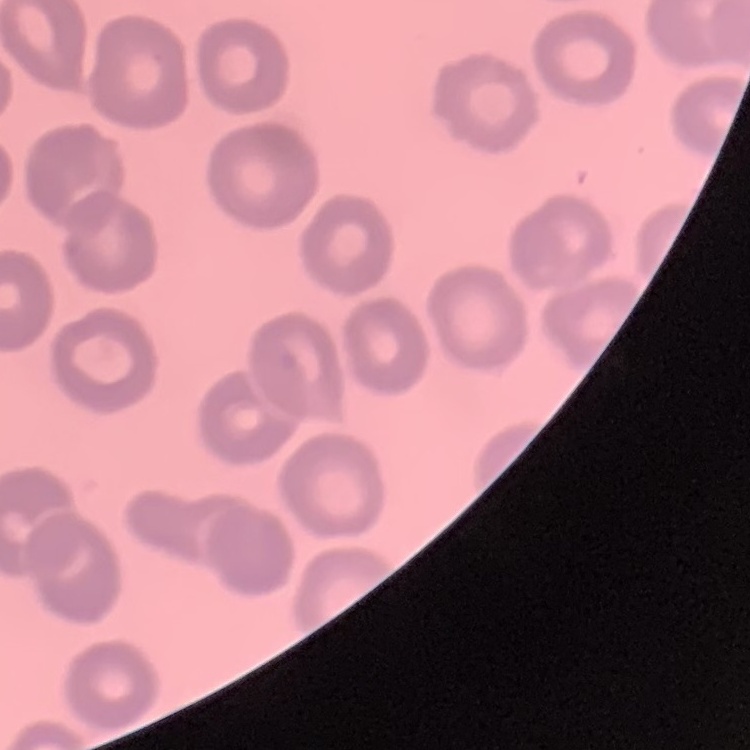
{
  "red_blood_cell_morphology": "no rouleaux formation",
  "image_type": "square crop of a larger photomicrograph",
  "preparation": "thin blood film",
  "stain": "Field's or Giemsa"
}